Report the malaria status of this cell.
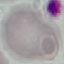

Uninfected.

{
  "preparation": "thin blood film",
  "image_type": "automatically extracted cell patch, resized to 64 × 64 pixels",
  "stain": "Giemsa",
  "capture": "smartphone through the microscope eyepiece"
}